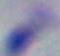
Summary:
  - Modality: photomicrograph
  - Magnification: 1000x
  - Identification: Toxoplasma gondii